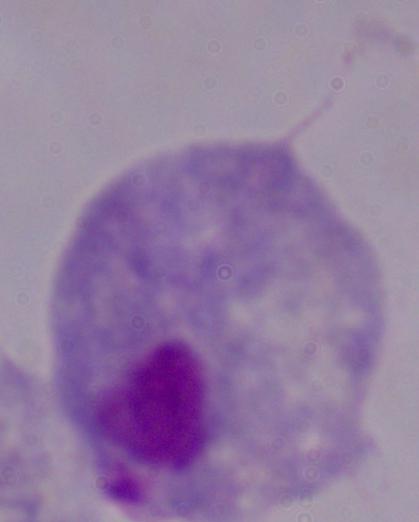

Summary:
  - Identification: trichomonad
  - Modality: micrograph
  - Magnification: 1000x